Describe the morphology of the red blood cells.
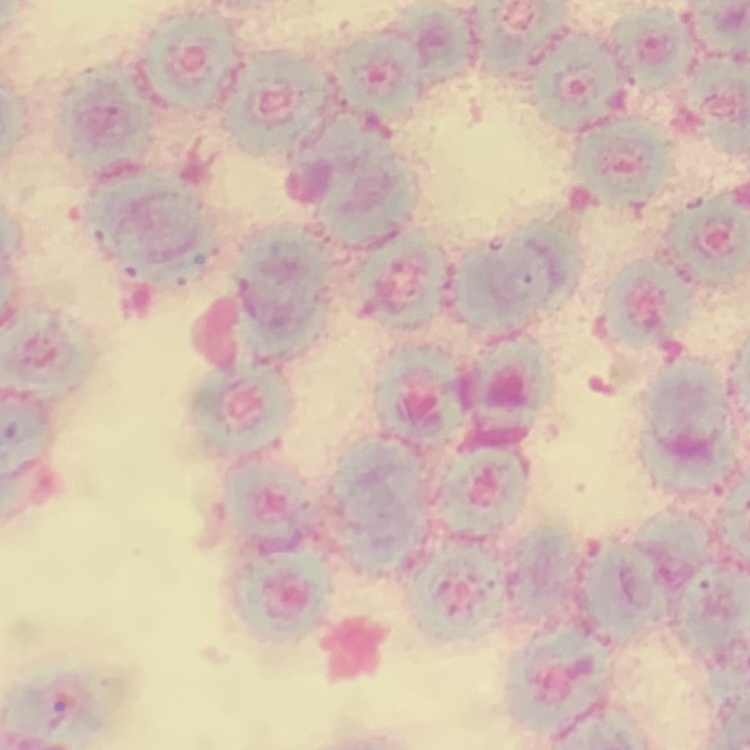
Rouleaux formation.

{
  "image_type": "one tile cut from a larger photomicrograph",
  "preparation": "thin blood smear",
  "stain": "Field's or Giemsa"
}